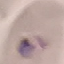
Result: malaria parasites detected. Thin blood smear. Giemsa-stained preparation. Photographed with a smartphone camera at the microscope eyepiece. Cell patch, automatically extracted from a larger field of view and resized to 64 × 64 pixels.